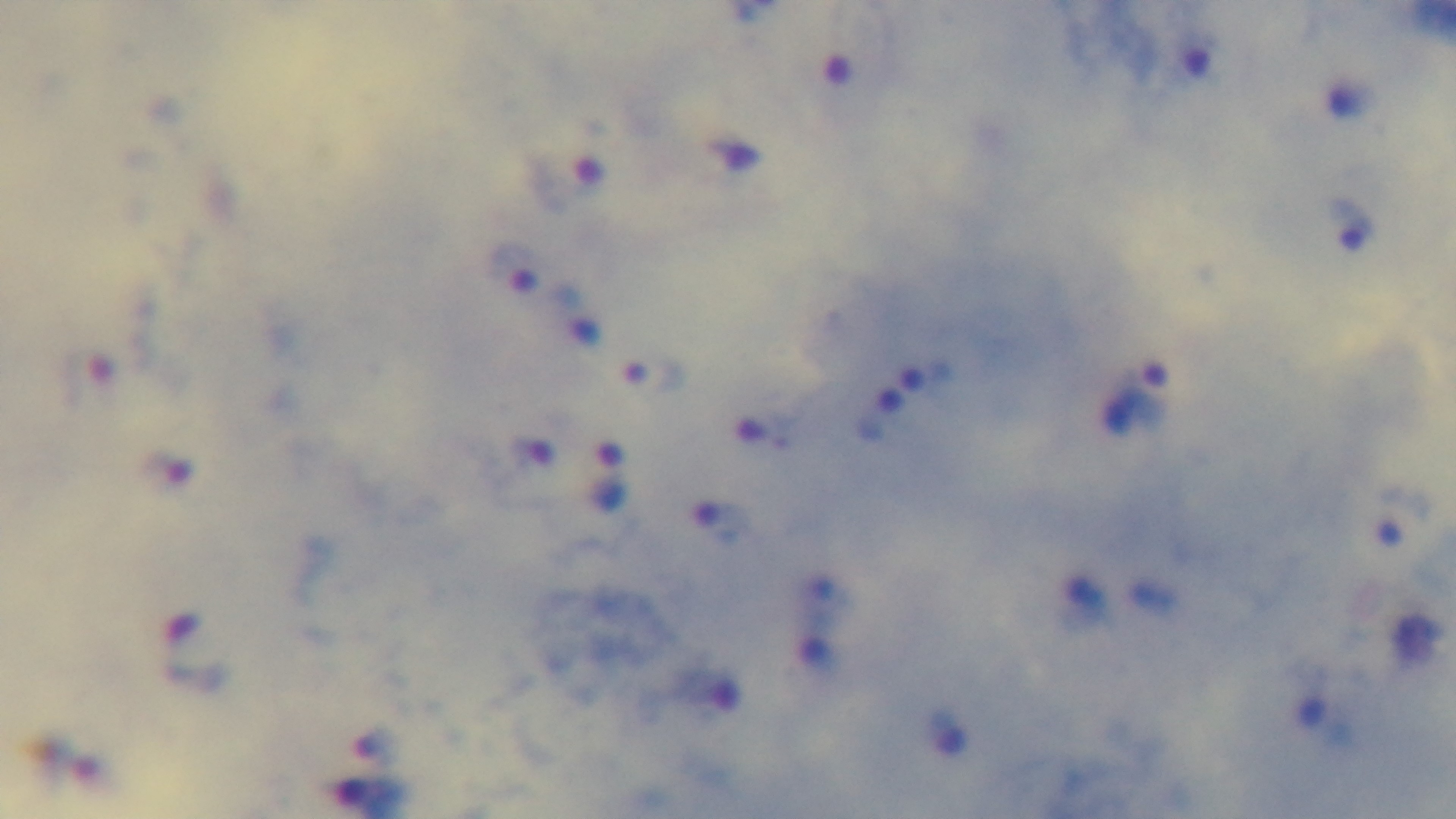
malaria status = infected
objective = 100x oil immersion
stain = Giemsa
capture = mounted 4K digital camera
modality = light microscopy
field of view = single
preparation = thick smear